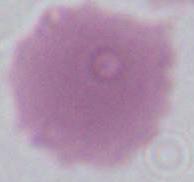

1000x magnification. An erythrocyte is seen. Micrograph.